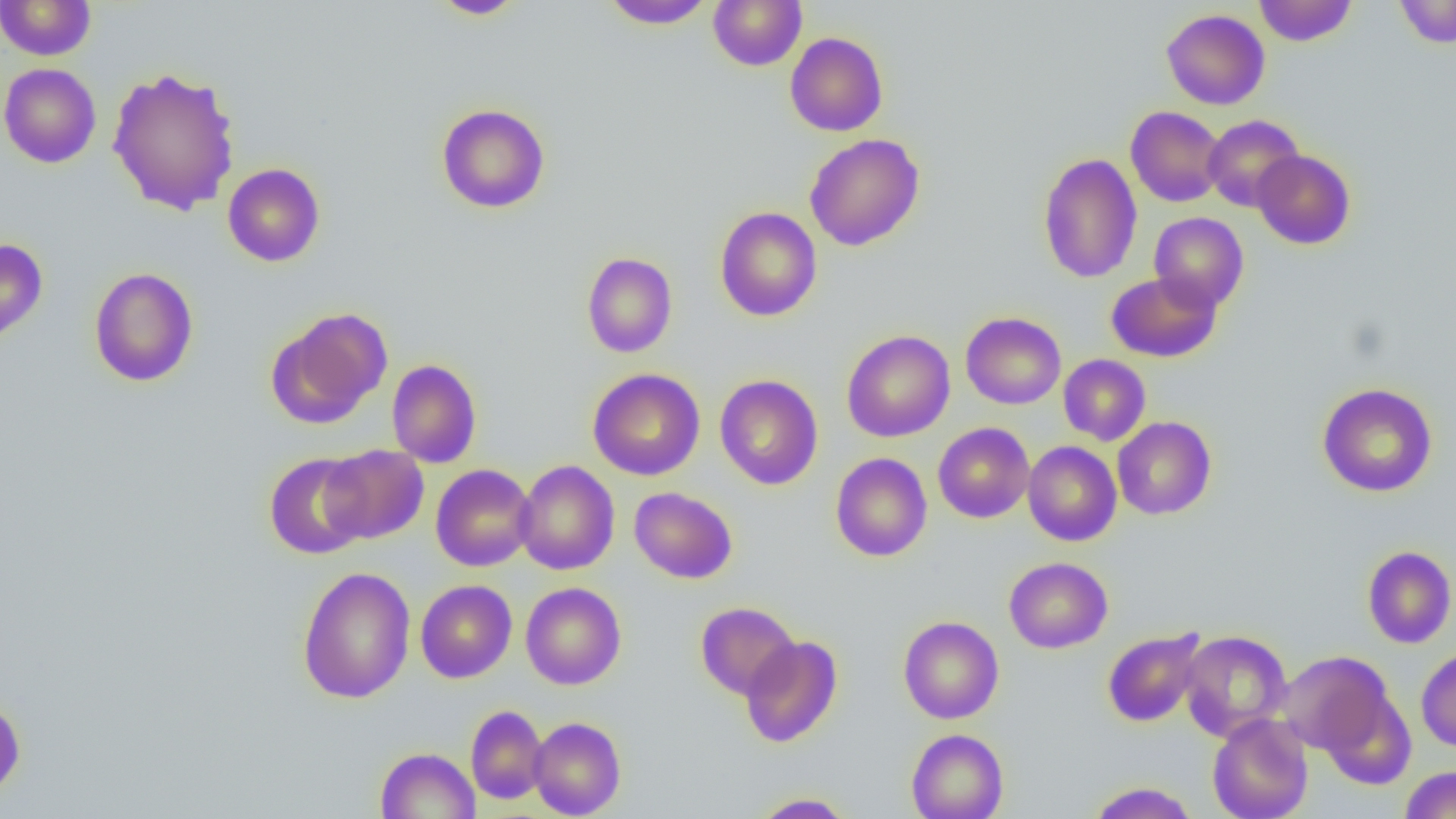
Approximate bounding boxes as [x1, y1, x2, y2] in pixels. Uninfected red blood cell locations: [430, 0, 527, 19], [601, 0, 715, 30], [708, 0, 807, 71], [1254, 0, 1357, 46], [1394, 0, 1456, 48], [0, 1, 97, 60], [1161, 9, 1270, 110], [785, 32, 888, 136], [0, 63, 102, 168], [107, 66, 241, 216], [436, 103, 550, 213], [1125, 106, 1226, 207], [1203, 115, 1305, 212], [804, 133, 924, 251], [1252, 149, 1356, 249], [1038, 153, 1142, 283], [222, 163, 325, 267], [714, 207, 822, 322], [1149, 213, 1248, 312], [0, 239, 48, 343], [581, 252, 678, 358], [89, 267, 199, 387], [1105, 272, 1222, 362], [269, 307, 393, 427], [961, 311, 1066, 409], [842, 330, 955, 442], [1058, 354, 1151, 446], [387, 359, 482, 468], [588, 368, 705, 480], [714, 374, 823, 490], [1317, 383, 1438, 497], [1112, 417, 1216, 520], [933, 422, 1034, 523], [1023, 441, 1121, 546], [320, 445, 429, 543], [263, 451, 371, 560], [830, 452, 932, 561], [514, 460, 619, 575], [431, 464, 536, 571], [629, 486, 737, 584], [1362, 545, 1456, 648], [1004, 557, 1113, 653], [297, 566, 416, 704], [415, 579, 517, 683], [520, 582, 626, 690], [695, 601, 800, 700], [898, 616, 1004, 724], [1102, 627, 1207, 728], [1179, 630, 1291, 741], [740, 636, 843, 747], [1416, 647, 1456, 752], [1277, 651, 1394, 755], [1318, 687, 1417, 788], [0, 694, 26, 801], [466, 705, 548, 805], [1207, 714, 1313, 819], [528, 716, 626, 818], [906, 728, 1009, 819], [375, 747, 480, 819], [1400, 766, 1456, 819], [1087, 781, 1199, 819], [751, 792, 856, 818]. Slide-level diagnosis: no evidence of blood parasites. Image is 1456×819 pixels. Single field of view. Optical microscopy. Thin blood smear. 1000x magnification.